Report the malaria status of this cell.
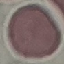

It is uninfected.

Summary:
  - Preparation: thin blood film
  - Stain: Giemsa
  - Capture: smartphone through the microscope eyepiece
  - Image type: automatically extracted cell patch, resized to 64 × 64 pixels